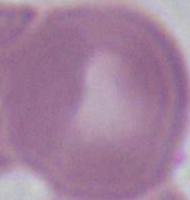
magnification = 1000x
modality = photomicrograph
identification = red blood cell